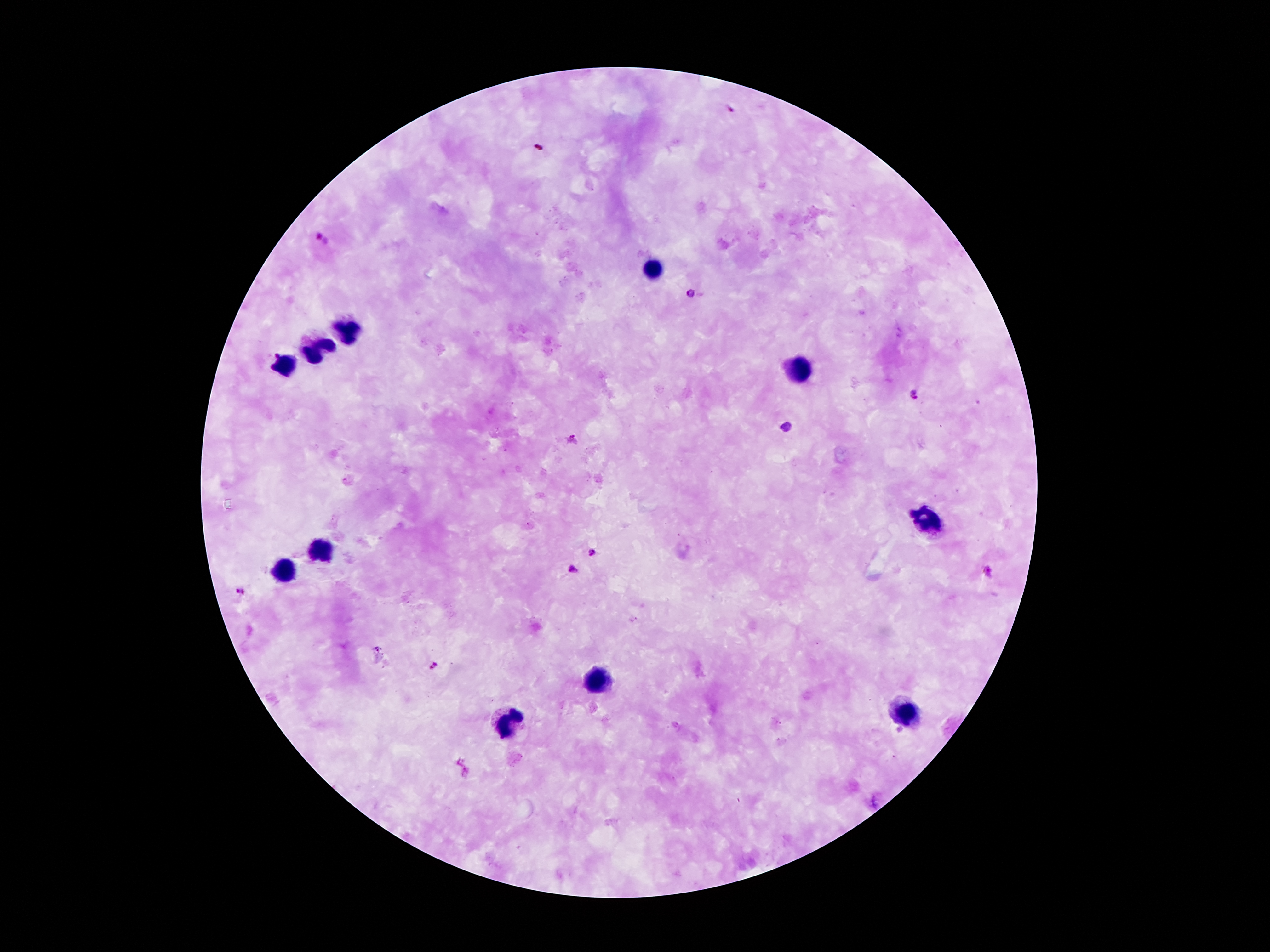

Approximate centers as [x, y] in pixels.
Summary:
  - Leukocyte locations: [654, 269], [347, 333], [314, 350], [280, 364], [797, 370], [923, 518], [318, 549], [282, 569], [597, 677], [906, 715], [509, 718]
  - Malaria parasite locations: [729, 109], [537, 146], [322, 241], [690, 293], [914, 396], [786, 426], [574, 440], [590, 554], [572, 569], [987, 571], [240, 591], [378, 647], [435, 665]
  - Preparation: thick peripheral-blood smear
  - Magnification: 100x
  - Image size: 1270×952 pixels
  - Patient malaria status: infected with Plasmodium falciparum
  - Capture: smartphone camera through the microscope eyepiece
  - Field of view: single
  - Stain: Giemsa